Classify this cell by malaria status.
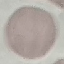
It is uninfected.

Cell patch, automatically extracted from a larger field of view and resized to 64 × 64 pixels. Acquired by smartphone through the microscope eyepiece. Thin blood film. Giemsa-stained preparation.